Assess this cell for malaria.
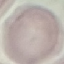

It is uninfected.

capture = smartphone camera at the microscope eyepiece
stain = Giemsa
preparation = thin smear
image type = automatically extracted cell patch, resized to 64 × 64 pixels